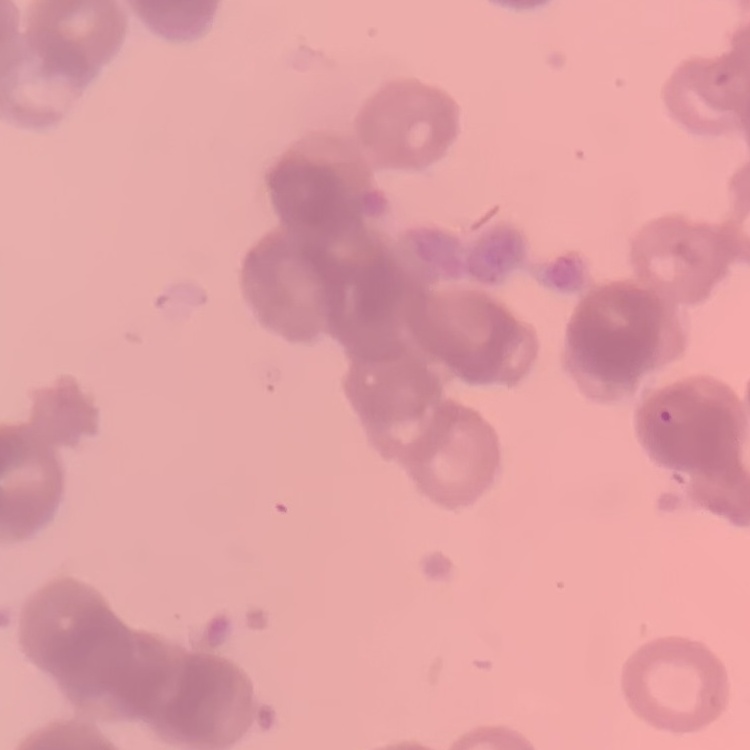
Summary:
  - Erythrocyte morphology: rouleaux formation
  - Stain: Field's or Giemsa
  - Image type: square crop of a larger photomicrograph
  - Preparation: thin blood smear